Point out each Plasmodium parasite and each leukocyte.
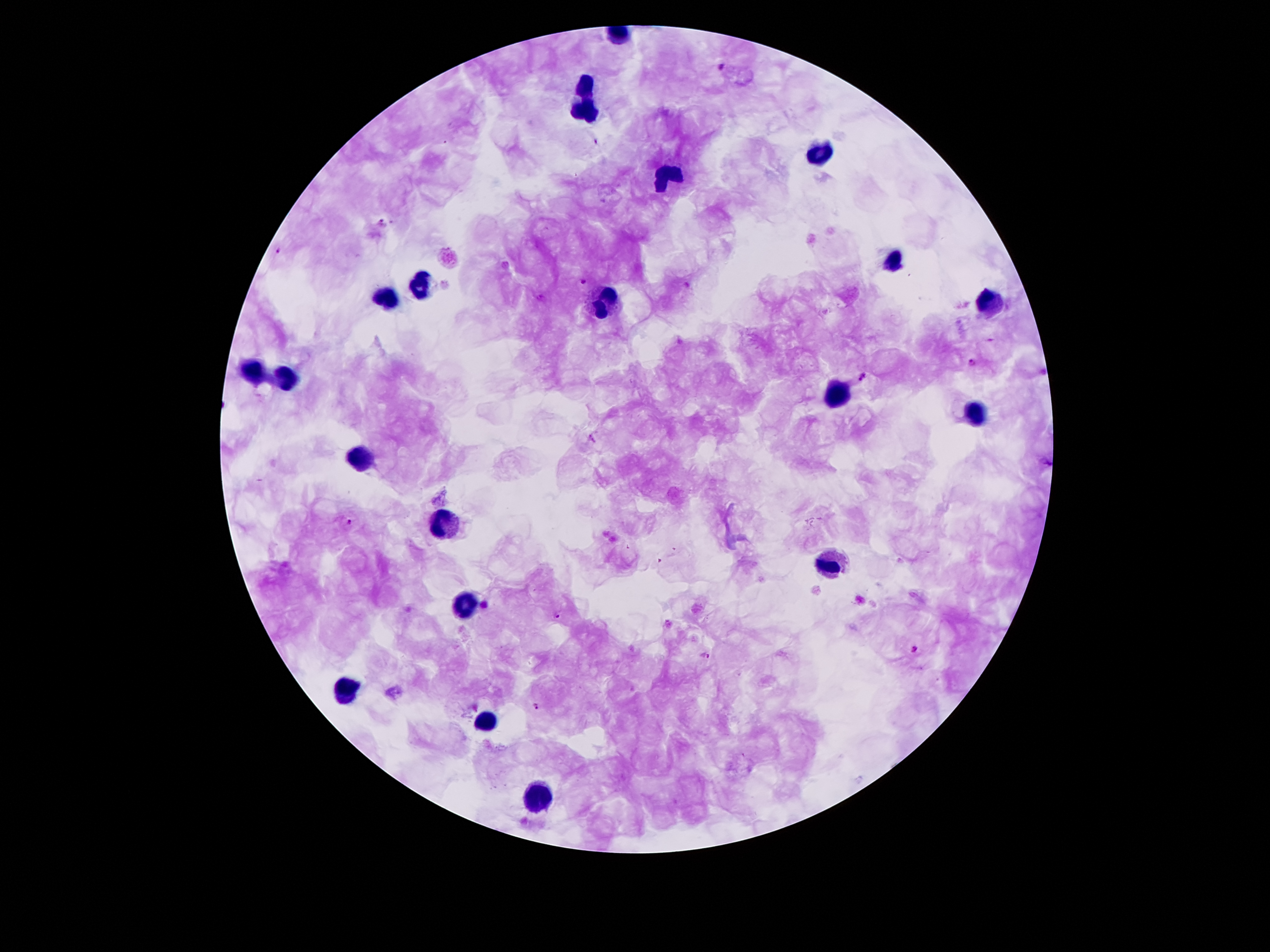
Approximate object centers, in pixels from the top-left corner.
Plasmodium parasites: (x=721, y=66), (x=596, y=142), (x=382, y=222), (x=279, y=252), (x=583, y=280), (x=971, y=363), (x=863, y=376), (x=349, y=522), (x=556, y=615), (x=914, y=650), (x=706, y=655), (x=537, y=707).
Leukocytes: (x=587, y=82), (x=585, y=112), (x=819, y=154), (x=672, y=179), (x=893, y=262), (x=424, y=284), (x=388, y=297), (x=604, y=298), (x=989, y=304), (x=249, y=371), (x=287, y=377), (x=839, y=396), (x=973, y=414), (x=362, y=456), (x=443, y=524), (x=831, y=567), (x=465, y=604), (x=345, y=691), (x=487, y=719), (x=539, y=797).

Thick blood smear. Smartphone photograph taken through the microscope eyepiece. Patient malaria status: positive for Plasmodium falciparum. 100x magnification. Image is 1270×952 pixels. Giemsa-stained preparation. Single field of view.